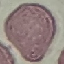
Summary:
  - Result: negative for malaria parasites
  - Capture: smartphone camera at the microscope eyepiece
  - Stain: Giemsa
  - Image type: automatically extracted cell patch, resized to 64 × 64 pixels
  - Preparation: thin smear